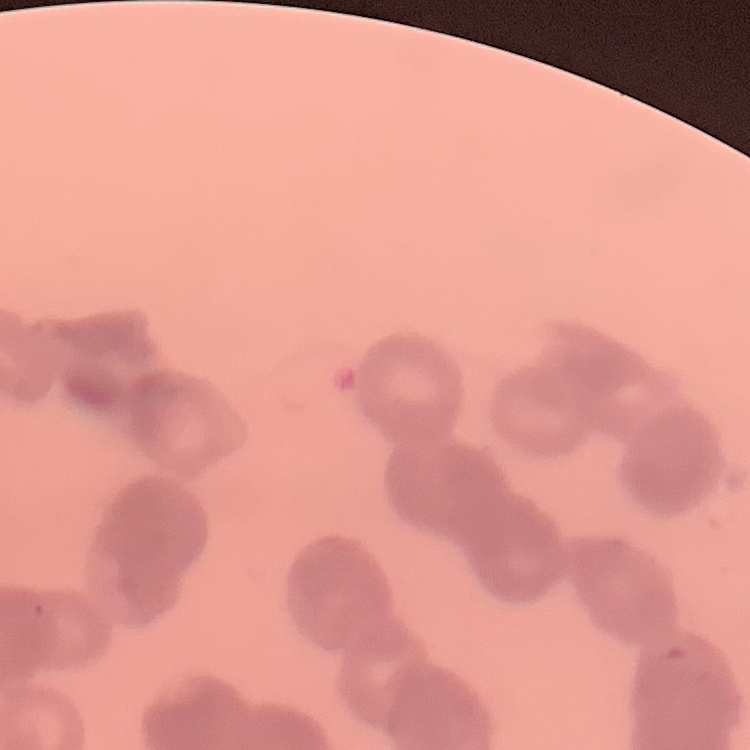

Summary:
  - Red blood cell morphology: rouleaux formation
  - Preparation: thin blood smear
  - Image type: square crop of a larger photomicrograph
  - Stain: Field's or Giemsa